Identify the parasite.
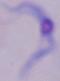

A trypanosome.

Summary:
  - Magnification: 1000x
  - Modality: micrograph